Name the parasite shown.
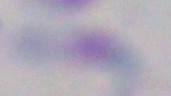
This is Toxoplasma gondii.

Summary:
  - Modality: micrograph
  - Magnification: 1000x